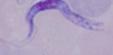

Summary:
  - Modality: micrograph
  - Magnification: 1000x
  - Identification: trypanosome